Assess this cell for malaria.
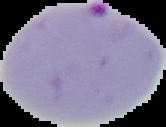
It is parasitized.

{
  "image_type": "segmented cell region on a black background",
  "preparation": "thin blood film",
  "image_size": "166×127 pixels"
}